Locate every leukocyte (white blood cell).
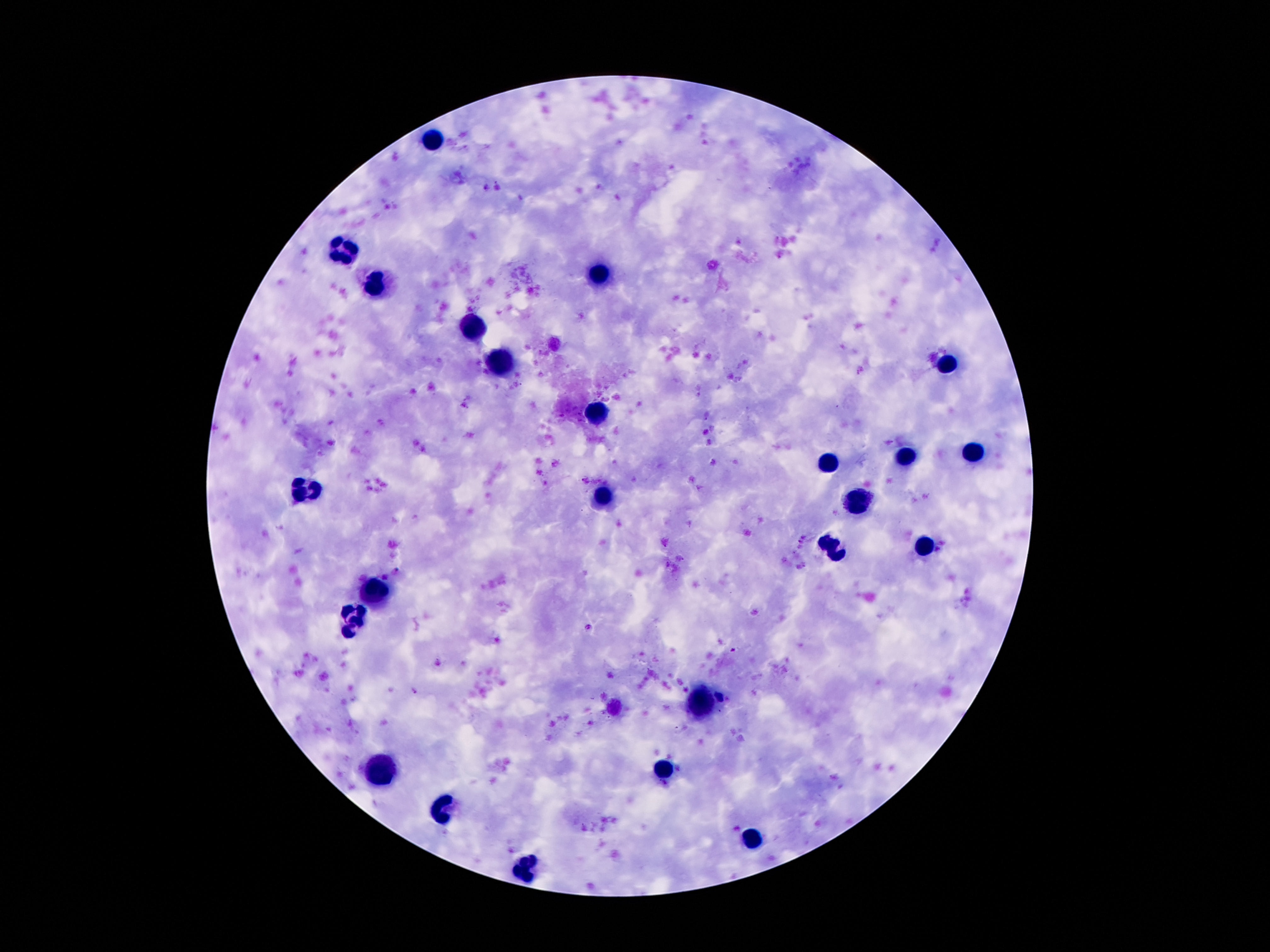
Approximate centers as (x, y) in pixels.
Leukocytes: (434, 140), (340, 252), (599, 274), (377, 287), (473, 323), (500, 364), (951, 364), (597, 412), (974, 452), (906, 456), (829, 461), (305, 490), (602, 497), (857, 500), (924, 544), (833, 547), (375, 591), (351, 617), (702, 702), (383, 767), (662, 767), (447, 807), (756, 839), (526, 870).

Giemsa stain. Single field of view. Image is 1270×952 pixels. 100x magnification. Thick peripheral-blood smear. Patient malaria status: uninfected. Smartphone photograph taken through the microscope eyepiece.